State which parasite is depicted.
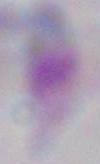

Toxoplasma gondii.

Summary:
  - Magnification: 1000x
  - Modality: micrograph